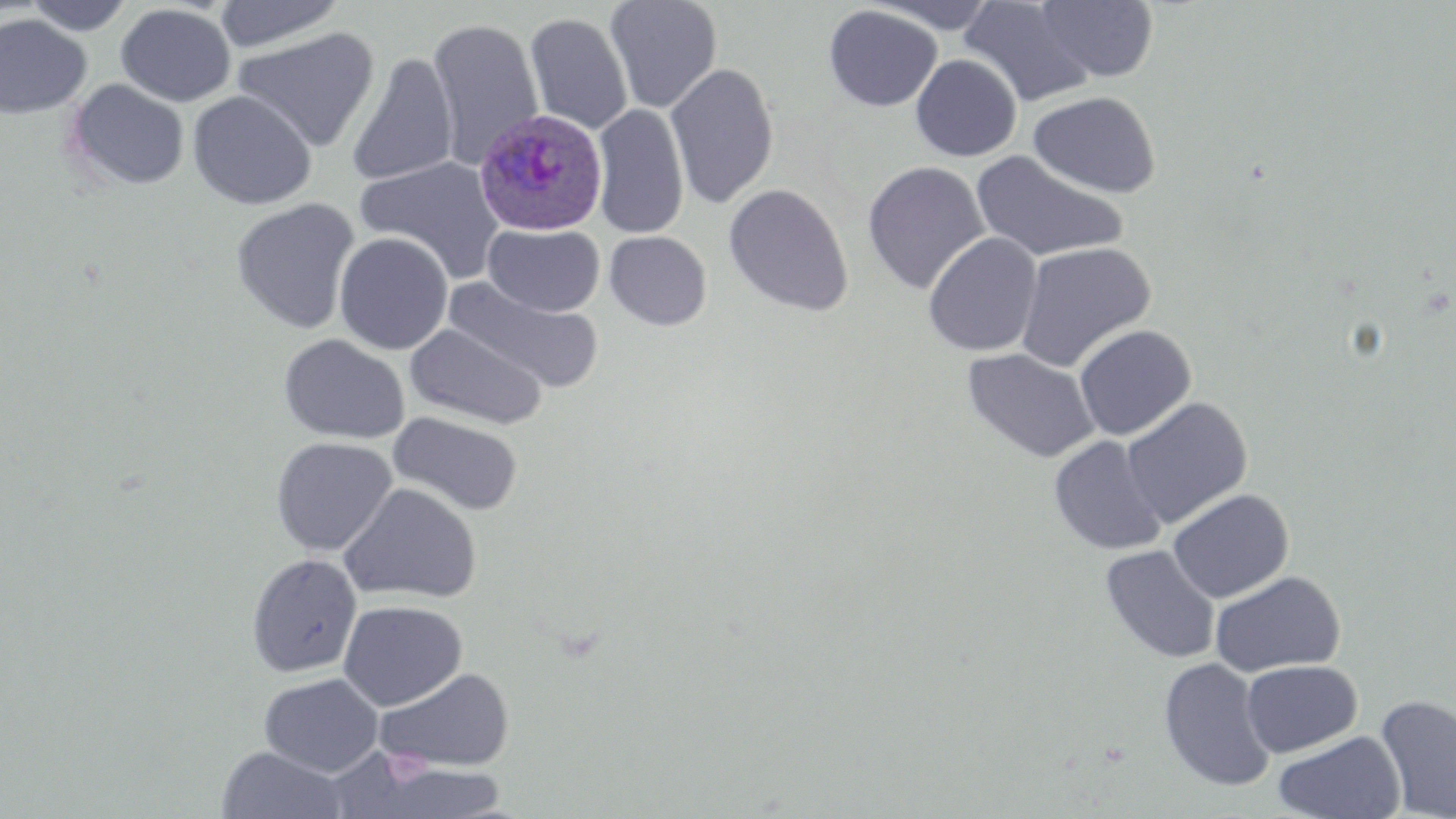
Approximate bounding boxes as [x1, y1, x2, y2] in pixels. Plasmodium ovale-infected red blood cell locations: [474, 109, 607, 236]. Uninfected red blood cell locations: [22, 0, 132, 35], [213, 0, 345, 53], [604, 0, 723, 113], [866, 0, 1003, 34], [959, 1, 1097, 108], [1036, 1, 1159, 82], [115, 3, 237, 107], [823, 5, 942, 111], [524, 12, 633, 135], [0, 14, 93, 119], [427, 17, 544, 168], [231, 27, 380, 152], [346, 53, 459, 186], [911, 54, 1022, 161], [666, 62, 779, 209], [64, 78, 191, 192], [187, 90, 317, 210], [1027, 90, 1160, 197], [592, 103, 689, 239], [971, 150, 1129, 264], [355, 156, 507, 283], [862, 160, 991, 295], [723, 183, 854, 316], [231, 198, 360, 334], [483, 223, 605, 316], [605, 231, 712, 330], [334, 232, 453, 354], [922, 232, 1043, 357], [1014, 240, 1157, 373], [444, 277, 604, 395], [405, 321, 549, 430], [1073, 324, 1197, 440], [278, 333, 410, 445], [962, 347, 1100, 463], [1121, 397, 1252, 529], [387, 412, 524, 516], [1048, 435, 1168, 555], [270, 436, 397, 555], [339, 483, 482, 604], [1168, 488, 1294, 603], [1100, 545, 1221, 664], [246, 552, 362, 678], [1210, 570, 1346, 677], [338, 600, 467, 711], [1158, 657, 1277, 792], [1241, 660, 1362, 757], [374, 667, 515, 773], [258, 673, 384, 777], [1376, 694, 1456, 818], [1272, 730, 1406, 819], [216, 746, 349, 818], [359, 762, 514, 819]. Slide-level diagnosis: Plasmodium ovale. Single field of view. Image is 1456×819 pixels. Light microscopy. May-Grünwald-Giemsa stain. Thin blood film. Captured at 1000x magnification.